Locate every white blood cell.
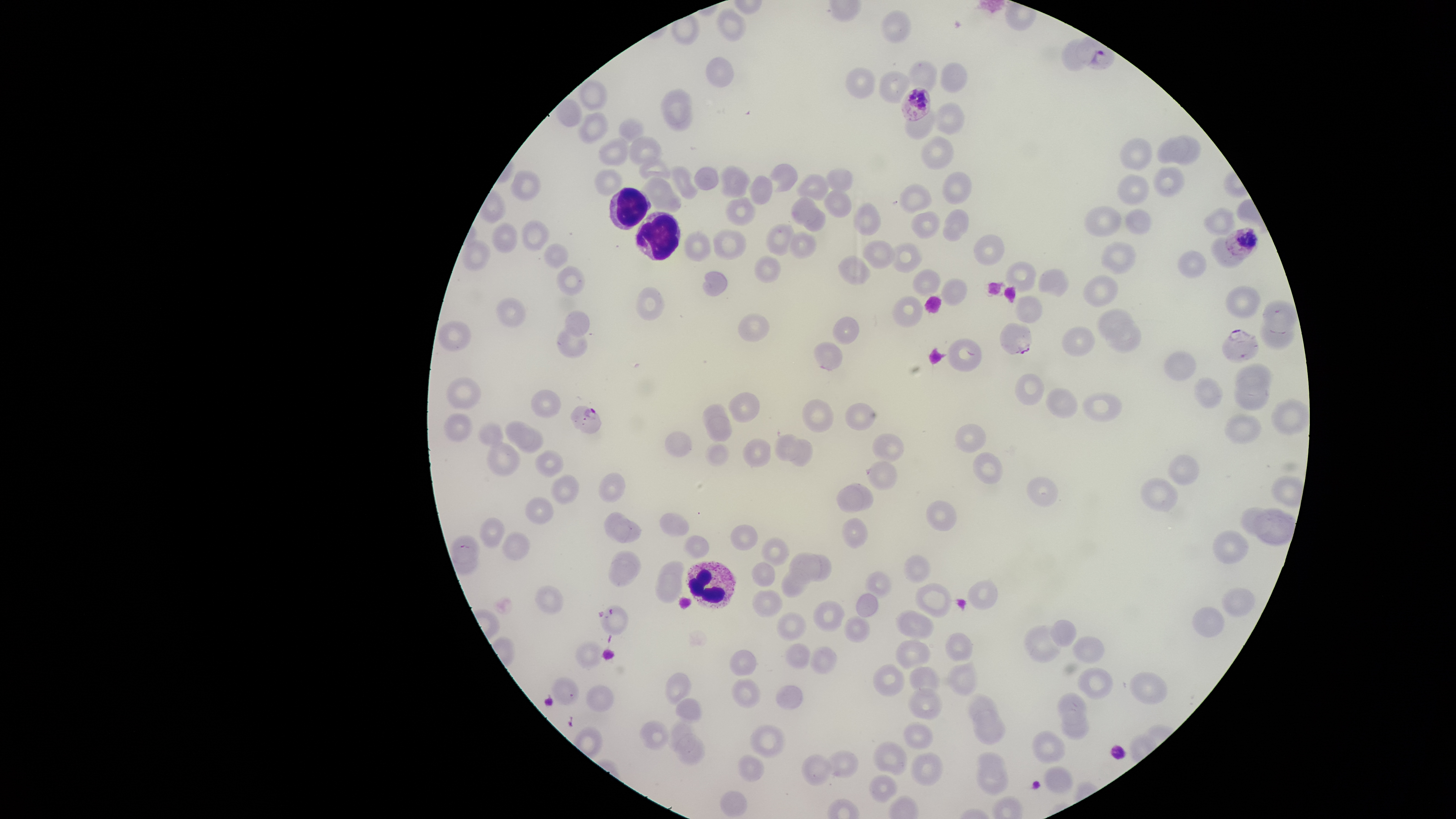

Approximate bounding boxes as {left, top, right, bottom} in pixels.
White blood cells: {609, 187, 651, 230}, {634, 211, 681, 261}, {685, 560, 737, 609}.

Approximate bounding boxes as {left, top, right, bottom} in pixels. Parasitized red blood cells: {900, 87, 931, 122}, {1223, 226, 1259, 260}, {1000, 322, 1032, 355}, {1222, 328, 1259, 363}, {570, 405, 602, 434}. Uninfected red blood cells: {718, 7, 747, 42}, {880, 9, 912, 44}, {705, 56, 735, 88}, {908, 59, 938, 92}, {940, 61, 969, 92}, {844, 67, 876, 99}, {878, 70, 911, 105}, {577, 77, 608, 111}, {661, 87, 693, 124}, {553, 98, 584, 127}, {665, 101, 694, 133}, {928, 103, 965, 136}, {905, 109, 934, 141}, {577, 112, 609, 145}, {618, 117, 645, 144}, {1171, 134, 1201, 165}, {627, 135, 662, 166}, {921, 135, 954, 170}, {597, 136, 629, 166}, {1118, 136, 1152, 171}, {1157, 136, 1190, 164}, {638, 157, 671, 180}, {768, 163, 798, 192}, {670, 164, 699, 201}, {693, 165, 720, 191}, {719, 165, 751, 198}, {1152, 166, 1185, 198}, {825, 167, 854, 192}, {594, 168, 623, 195}, {510, 170, 542, 201}, {941, 171, 973, 205}, {795, 173, 830, 201}, {1116, 174, 1150, 206}, {748, 175, 773, 205}, {639, 176, 683, 215}, {898, 183, 932, 214}, {823, 188, 852, 218}, {724, 196, 756, 226}, {791, 196, 817, 227}, {852, 202, 881, 236}, {1084, 205, 1122, 237}, {804, 207, 827, 232}, {1202, 207, 1236, 237}, {942, 208, 969, 242}, {1124, 208, 1152, 236}, {909, 211, 941, 239}, {521, 219, 550, 252}, {490, 222, 519, 254}, {765, 222, 795, 256}, {712, 228, 746, 260}, {787, 230, 817, 259}, {684, 231, 712, 262}, {972, 233, 1005, 266}, {1210, 236, 1245, 268}, {460, 238, 491, 272}, {861, 240, 896, 270}, {1100, 241, 1136, 274}, {889, 242, 923, 273}, {543, 243, 569, 269}, {1177, 250, 1207, 278}, {753, 255, 782, 284}, {837, 255, 872, 286}, {1005, 261, 1036, 293}, {556, 265, 585, 296}, {912, 268, 941, 296}, {1038, 268, 1069, 298}, {701, 271, 728, 296}, {1082, 275, 1119, 307}, {940, 277, 968, 307}, {1223, 284, 1262, 319}, {635, 287, 665, 321}, {891, 295, 923, 328}, {1014, 295, 1043, 324}, {495, 297, 526, 328}, {1261, 299, 1298, 333}, {1097, 308, 1133, 340}, {564, 309, 590, 337}, {737, 313, 770, 342}, {832, 315, 860, 345}, {1259, 317, 1295, 349}, {1104, 319, 1142, 353}, {437, 320, 472, 353}, {556, 326, 588, 359}, {1061, 326, 1096, 357}, {947, 337, 983, 373}, {813, 341, 843, 371}, {1163, 350, 1197, 381}, {1234, 362, 1271, 396}, {1014, 373, 1045, 405}, {1234, 375, 1270, 411}, {1193, 376, 1224, 409}, {446, 377, 482, 410}, {1045, 387, 1079, 419}, {531, 388, 561, 417}, {727, 392, 759, 422}, {1081, 392, 1123, 421}, {1271, 398, 1309, 437}, {802, 399, 834, 433}, {844, 402, 876, 431}, {702, 403, 729, 433}, {1224, 412, 1262, 445}, {442, 413, 473, 442}, {706, 415, 733, 442}, {504, 420, 534, 448}, {476, 423, 504, 448}, {954, 423, 987, 453}, {515, 427, 544, 454}, {664, 430, 692, 458}, {773, 433, 803, 461}, {871, 433, 905, 463}, {741, 437, 772, 468}, {789, 437, 813, 468}, {486, 441, 521, 477}, {704, 441, 730, 467}, {535, 449, 564, 478}, {972, 451, 1003, 484}, {1168, 453, 1200, 486}, {865, 460, 898, 490}, {598, 472, 626, 503}, {550, 474, 578, 505}, {1026, 476, 1058, 507}, {1139, 477, 1178, 511}, {845, 482, 873, 511}, {836, 485, 865, 514}, {524, 495, 554, 526}, {925, 499, 957, 532}, {1239, 507, 1272, 537}, {1253, 508, 1297, 546}, {603, 511, 632, 543}, {659, 512, 690, 538}, {478, 517, 505, 549}, {841, 517, 867, 549}, {611, 518, 643, 543}, {730, 524, 758, 551}, {1213, 529, 1250, 564}, {501, 530, 531, 561}, {449, 534, 480, 565}, {683, 535, 710, 560}, {760, 537, 790, 567}, {451, 547, 480, 576}, {610, 550, 642, 580}, {788, 551, 822, 585}, {808, 554, 832, 581}, {903, 554, 931, 583}, {608, 559, 638, 588}, {658, 560, 685, 584}, {750, 562, 776, 586}, {781, 568, 810, 597}, {864, 571, 892, 599}, {654, 574, 683, 603}, {967, 580, 999, 610}, {914, 582, 952, 617}, {534, 585, 565, 614}, {1222, 587, 1257, 617}, {751, 589, 784, 618}, {855, 592, 879, 618}, {812, 601, 846, 632}, {599, 604, 629, 634}, {1191, 605, 1225, 637}, {894, 609, 935, 640}, {775, 612, 807, 641}, {843, 615, 871, 642}, {1049, 619, 1077, 647}, {1023, 624, 1061, 663}, {944, 631, 973, 662}, {1071, 635, 1106, 664}, {895, 639, 931, 670}, {575, 641, 602, 670}, {783, 643, 812, 669}, {809, 645, 838, 675}, {728, 649, 757, 676}, {946, 657, 978, 696}, {872, 663, 905, 697}, {908, 665, 940, 697}, {1076, 667, 1114, 700}, {1128, 671, 1168, 705}, {664, 672, 692, 706}, {549, 676, 578, 706}, {731, 678, 762, 707}, {586, 683, 615, 713}, {776, 684, 804, 710}, {907, 687, 943, 720}, {965, 692, 998, 725}, {1056, 692, 1088, 726}, {675, 698, 702, 723}, {973, 709, 1006, 745}, {1061, 712, 1089, 741}, {640, 719, 670, 750}, {667, 719, 696, 755}, {903, 721, 933, 749}, {749, 724, 787, 758}, {1032, 730, 1066, 764}, {675, 733, 705, 765}, {872, 740, 908, 776}, {823, 749, 859, 779}, {974, 751, 1007, 783}, {910, 752, 944, 787}, {801, 753, 832, 786}, {737, 754, 765, 782}, {1043, 765, 1074, 795}, {976, 766, 1009, 795}, {868, 774, 898, 803}, {720, 791, 748, 818}. One field of view of the specimen. Smartphone photograph through the microscope eyepiece. Giemsa-stained preparation. Thin blood film. Presence: malaria parasites detected. The visible region is circular. Species: Plasmodium falciparum. Image is 1456×819 pixels.